Describe the morphology of the red blood cells.
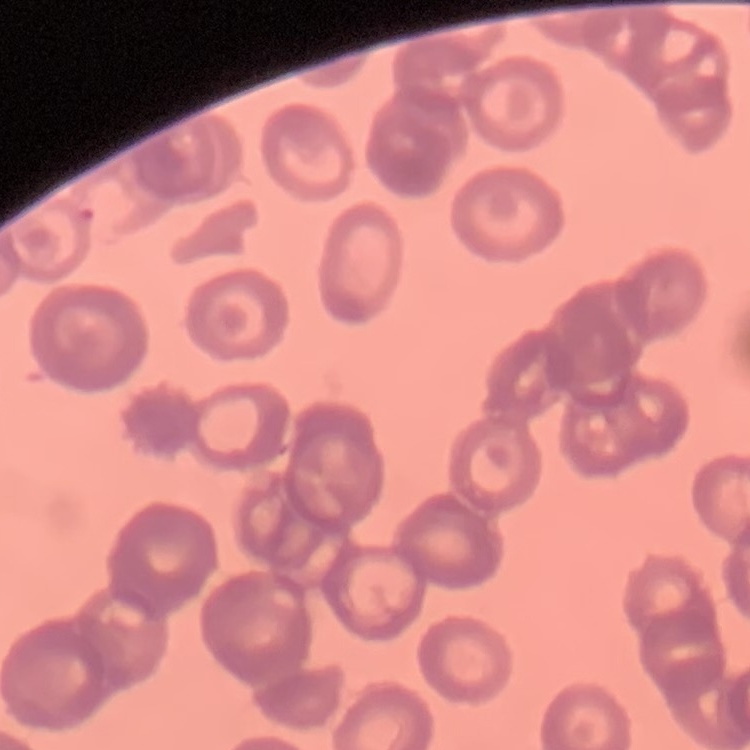
They show rouleaux formation.

Stained with either Field's or Giemsa. One tile cut from a larger photomicrograph. Thin peripheral smear.